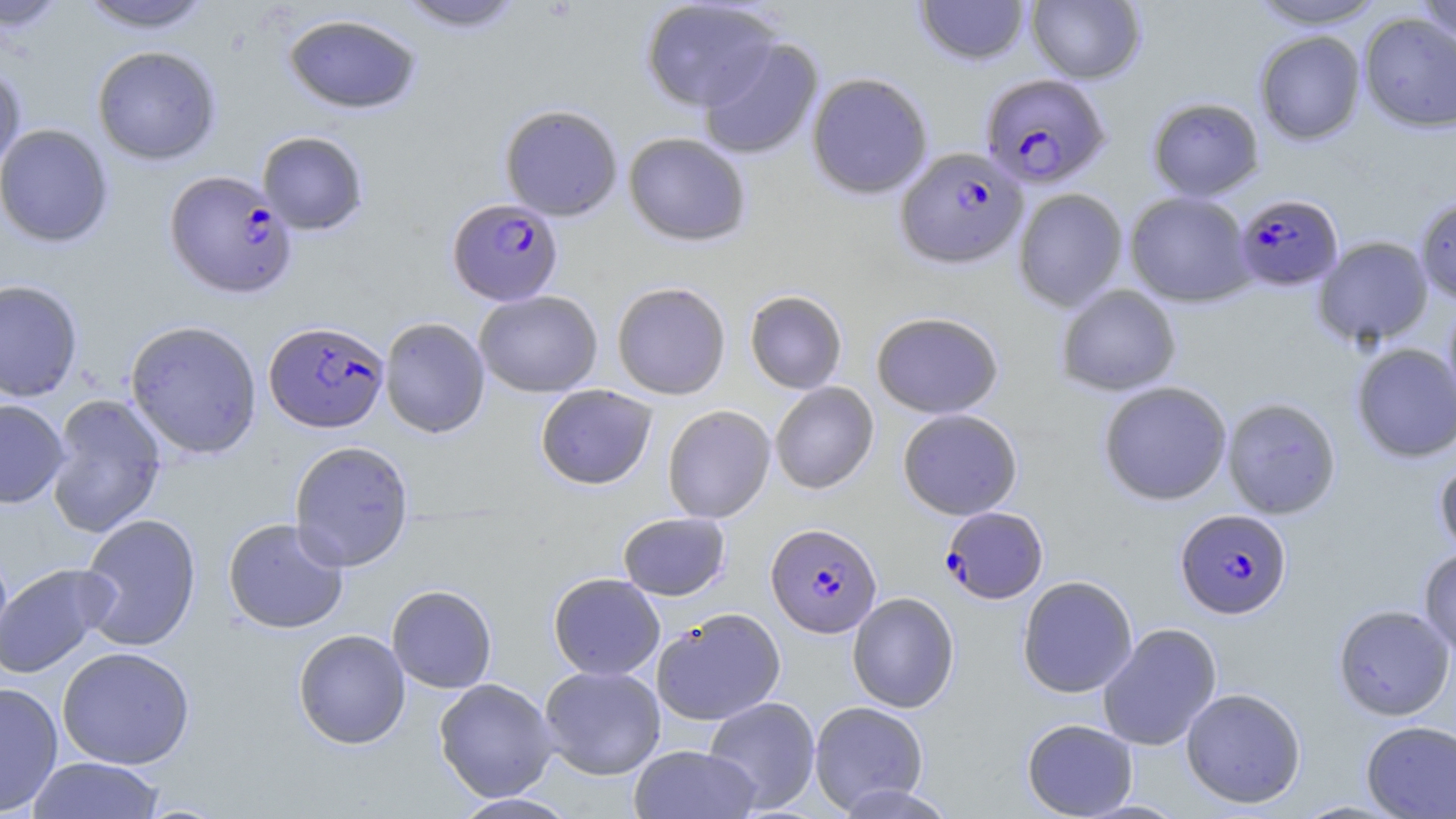

slide-level diagnosis = Plasmodium falciparum
magnification = 1000x
preparation = thin blood film
Plasmodium falciparum-infected red blood cell locations = approximate bounding boxes as [x1, y1, x2, y2] in pixels: [979, 73, 1110, 189], [895, 147, 1028, 270], [164, 170, 297, 299], [1234, 193, 1343, 292], [447, 198, 563, 306], [264, 321, 389, 433], [940, 506, 1048, 604], [1175, 509, 1291, 619], [766, 523, 882, 638]
modality = light microscopy
stain = May-Grünwald-Giemsa
uninfected red blood cell locations = approximate bounding boxes as [x1, y1, x2, y2] in pixels: [75, 0, 218, 33], [392, 0, 528, 33], [640, 0, 782, 112], [1026, 0, 1145, 84], [1247, 0, 1386, 29], [1414, 0, 1456, 45], [1, 1, 71, 34], [914, 1, 1031, 66], [283, 12, 422, 115], [1359, 13, 1456, 133], [1254, 30, 1366, 145], [698, 36, 823, 160], [92, 45, 221, 165], [0, 62, 26, 176], [807, 72, 933, 199], [1146, 97, 1264, 201], [499, 103, 623, 220], [0, 123, 114, 248], [257, 131, 369, 235], [623, 132, 751, 247], [1013, 188, 1128, 312], [1124, 191, 1255, 307], [1415, 195, 1456, 304], [1313, 236, 1433, 347], [0, 279, 83, 402], [611, 282, 731, 400], [1056, 285, 1181, 396], [474, 290, 603, 397], [744, 290, 848, 394], [1443, 297, 1456, 416], [871, 311, 1004, 418], [379, 317, 490, 439], [125, 320, 262, 459], [1351, 343, 1456, 463], [1098, 381, 1232, 506], [770, 382, 879, 495], [535, 384, 657, 490], [46, 394, 166, 538], [1222, 397, 1341, 519], [0, 399, 69, 509], [662, 405, 775, 523], [897, 409, 1023, 520], [288, 440, 414, 572], [1434, 457, 1456, 559], [617, 512, 731, 600], [77, 513, 202, 652], [223, 517, 349, 634], [1418, 548, 1456, 660], [0, 563, 116, 679], [548, 573, 665, 680], [1017, 575, 1138, 698], [386, 584, 497, 694], [847, 592, 960, 713], [1333, 604, 1455, 721], [651, 608, 786, 726], [1097, 623, 1222, 751], [293, 629, 410, 749], [56, 646, 195, 770], [539, 665, 666, 780], [434, 678, 559, 802], [0, 681, 63, 816], [1180, 687, 1306, 808], [703, 697, 820, 813], [809, 701, 929, 814], [1021, 719, 1138, 818], [1360, 720, 1456, 818], [629, 745, 761, 819], [27, 756, 165, 818], [833, 783, 958, 818], [451, 793, 579, 818]
field of view = one of a larger specimen
image size = 1456×819 pixels